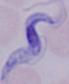
A trypanosome is shown. Photomicrograph. 1000x magnification.